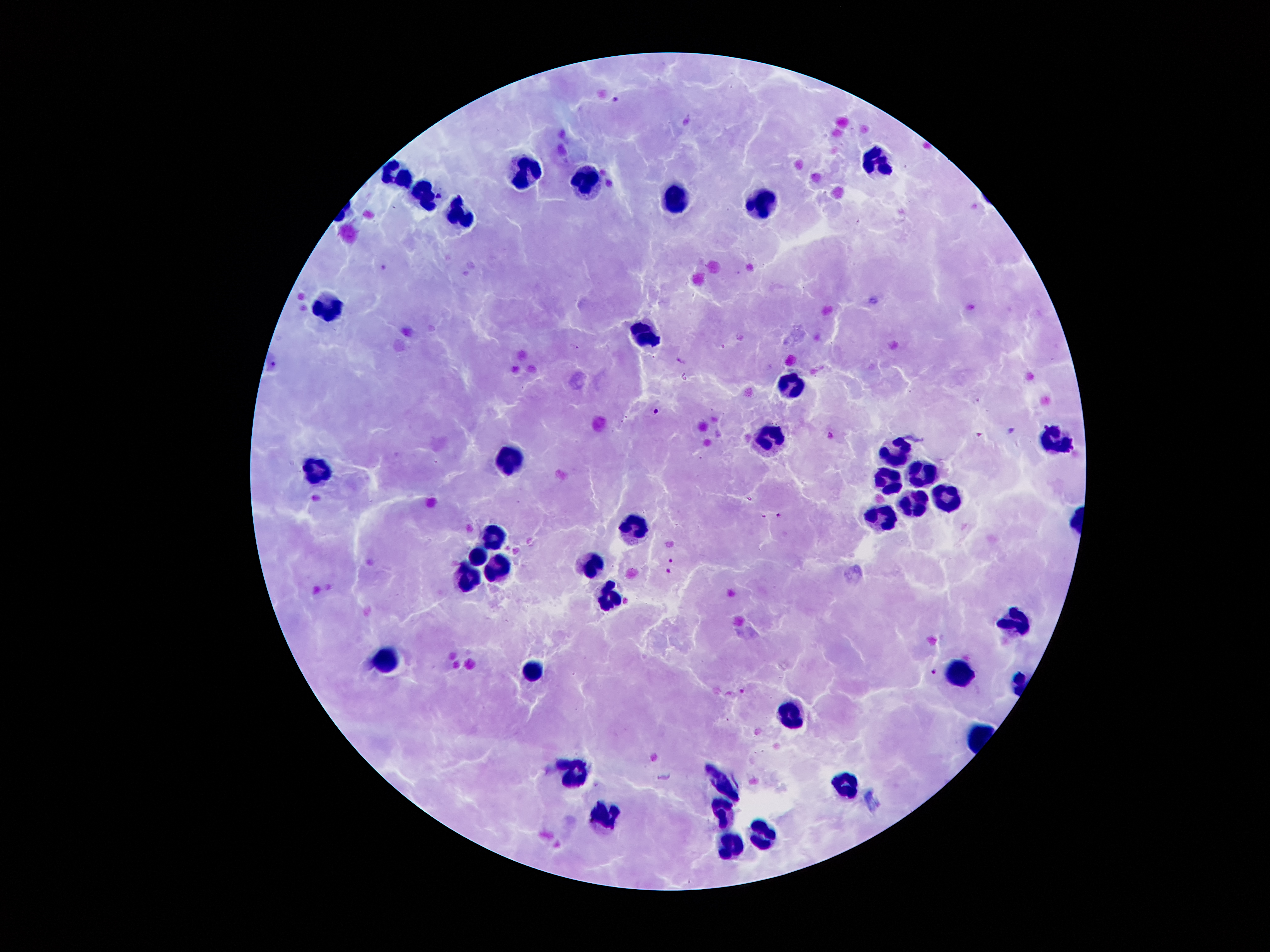

Approximate centers as (x, y) in pixels.
Summary:
  - Leukocyte locations: (883, 162), (530, 169), (395, 172), (582, 179), (430, 196), (671, 196), (760, 200), (461, 215), (333, 305), (648, 337), (792, 383), (774, 436), (1050, 440), (893, 449), (505, 457), (924, 472), (317, 473), (886, 479), (948, 499), (911, 503), (881, 518), (631, 525), (495, 535), (478, 557), (592, 565), (500, 568), (465, 580), (608, 597), (1012, 622), (388, 660), (533, 670), (963, 675), (793, 718), (577, 778), (845, 781), (722, 786), (601, 814), (722, 818), (759, 835), (728, 847)
  - Plasmodium parasite locations: (613, 99), (384, 266), (577, 348), (681, 362), (657, 411), (1012, 429), (777, 515), (764, 516), (671, 560), (667, 571), (932, 671), (743, 690)
  - Image size: 1270×952 pixels
  - Stain: Giemsa
  - Magnification: 100x
  - Field of view: single
  - Preparation: thick peripheral-blood smear
  - Patient malaria status: infected with Plasmodium falciparum
  - Capture: smartphone camera through the microscope eyepiece